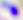
magnification = 400x
modality = micrograph
identification = Toxoplasma gondii